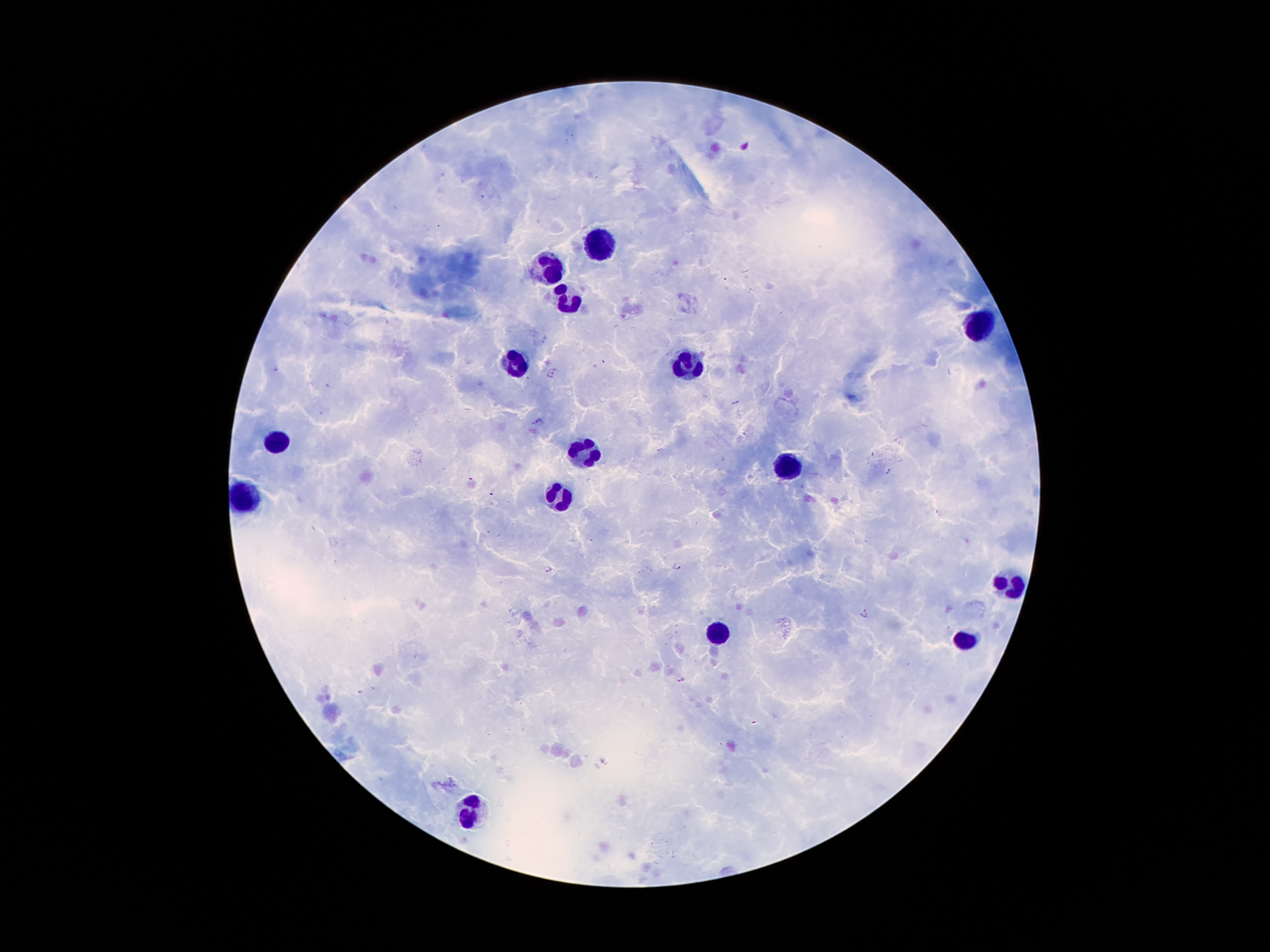

coordinate format = approximate centers as [x, y] in pixels
malaria parasite locations = [554, 373], [679, 566], [548, 569], [864, 614], [679, 679]
leukocyte locations = [602, 249], [550, 268], [563, 297], [980, 325], [518, 360], [689, 367], [275, 443], [586, 453], [789, 468], [250, 495], [560, 501], [1007, 585], [722, 634], [961, 640], [470, 812]
image size = 1270×952 pixels
stain = Giemsa
preparation = thick peripheral-blood smear
field of view = one from this slide
magnification = 100x
capture = smartphone through the microscope eyepiece
patient malaria status = infected with Plasmodium falciparum